Outline each blood parasite and name the species.
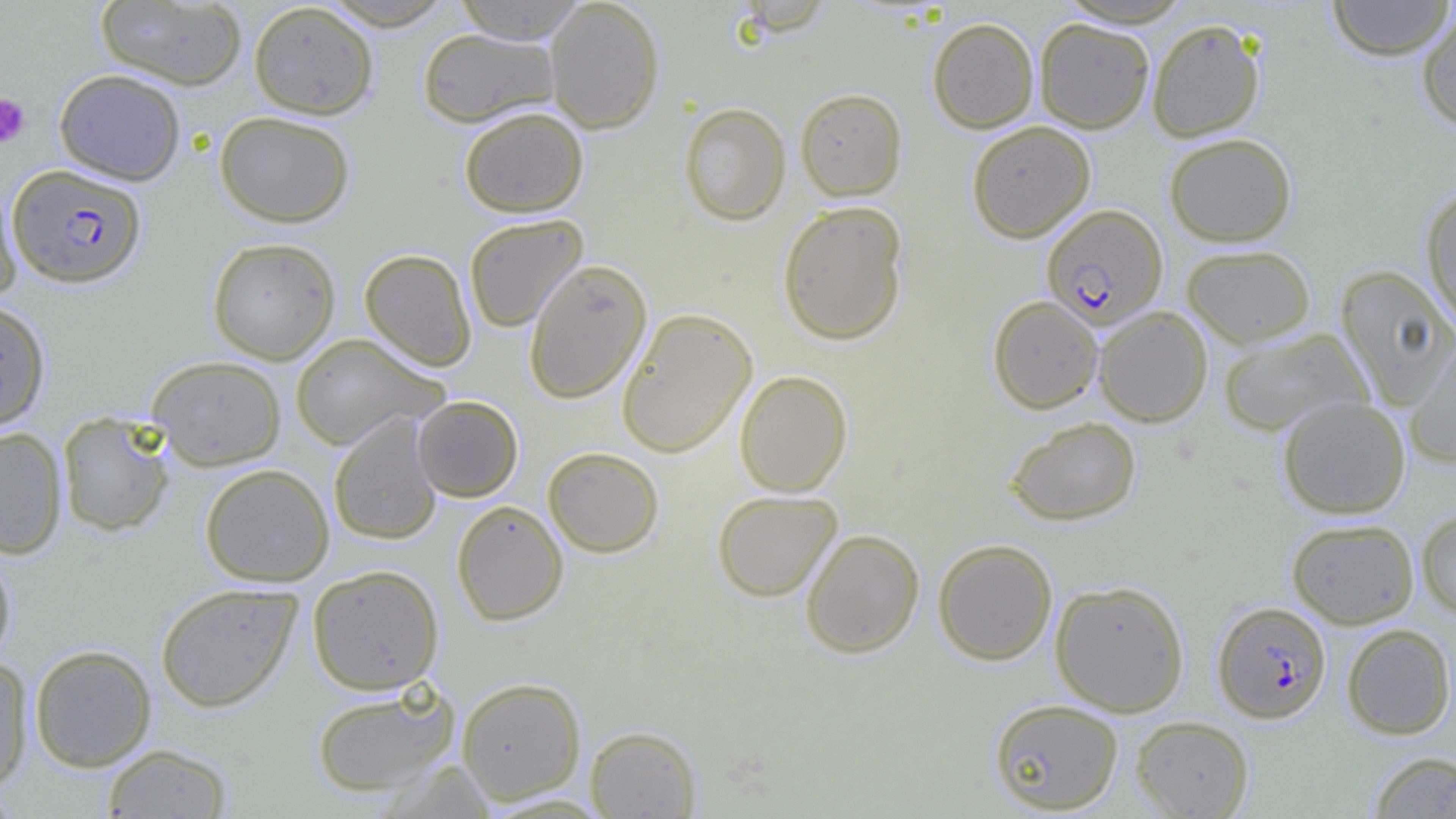

Approximate bounding boxes as (x1,y1)-(x2,y2) corner pairs in pixels.
Plasmodium falciparum-infected red blood cells: (7,164)-(147,288), (1040,204)-(1168,329), (1212,600)-(1331,723).
No Plasmodium ovale, Plasmodium malariae, Plasmodium vivax, Babesia divergens, or Trypanosoma brucei observed.

Summary:
  - Uninfected red blood cell locations: (318,0)-(459,31), (451,0)-(588,44), (544,0)-(665,134), (1326,0)-(1455,60), (95,1)-(247,89), (248,2)-(378,119), (1416,7)-(1456,130), (927,17)-(1039,133), (1034,17)-(1155,133), (1147,17)-(1265,142), (416,28)-(560,127), (54,68)-(186,185), (795,87)-(908,201), (678,102)-(791,226), (458,106)-(589,217), (214,110)-(356,228), (966,120)-(1095,242), (1163,133)-(1297,246), (0,179)-(23,301), (1420,185)-(1456,332), (777,200)-(909,345), (463,214)-(589,333), (207,236)-(341,364), (1181,244)-(1316,348), (359,248)-(477,371), (523,259)-(652,404), (1334,264)-(1456,408), (987,295)-(1103,414), (0,299)-(50,430), (1094,306)-(1213,427), (616,307)-(757,457), (1217,327)-(1372,438), (289,333)-(448,450), (1402,338)-(1456,467), (146,356)-(287,470), (734,369)-(853,496), (412,395)-(523,502), (1277,396)-(1411,519), (56,411)-(176,537), (328,413)-(443,546), (1003,416)-(1141,526), (0,427)-(68,559), (542,446)-(664,558), (200,463)-(335,586), (711,490)-(843,602), (451,500)-(569,626), (1415,507)-(1456,619), (1286,518)-(1419,628), (800,528)-(925,659), (932,538)-(1058,665), (0,549)-(18,669), (306,564)-(445,695), (1050,580)-(1189,716), (155,582)-(302,713), (1341,623)-(1455,740), (29,644)-(157,771), (0,656)-(34,792), (456,677)-(587,804), (310,686)-(459,798), (988,698)-(1124,814), (1131,716)-(1254,818), (585,725)-(702,818), (101,743)-(233,818), (1368,751)-(1456,818), (0,783)-(22,818)
  - Platelet locations: (0,93)-(31,148)
  - Slide-level diagnosis: Plasmodium falciparum
  - Magnification: 1000x
  - Preparation: thin blood smear
  - Modality: light microscopy
  - Image size: 1456×819 pixels
  - Field of view: single